Assess this cell for malaria.
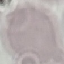
Uninfected.

{
  "preparation": "thin blood film",
  "capture": "smartphone through the microscope eyepiece",
  "image_type": "automatically extracted cell patch, resized to 64 × 64 pixels",
  "stain": "Giemsa"
}